Locate every Plasmodium parasite.
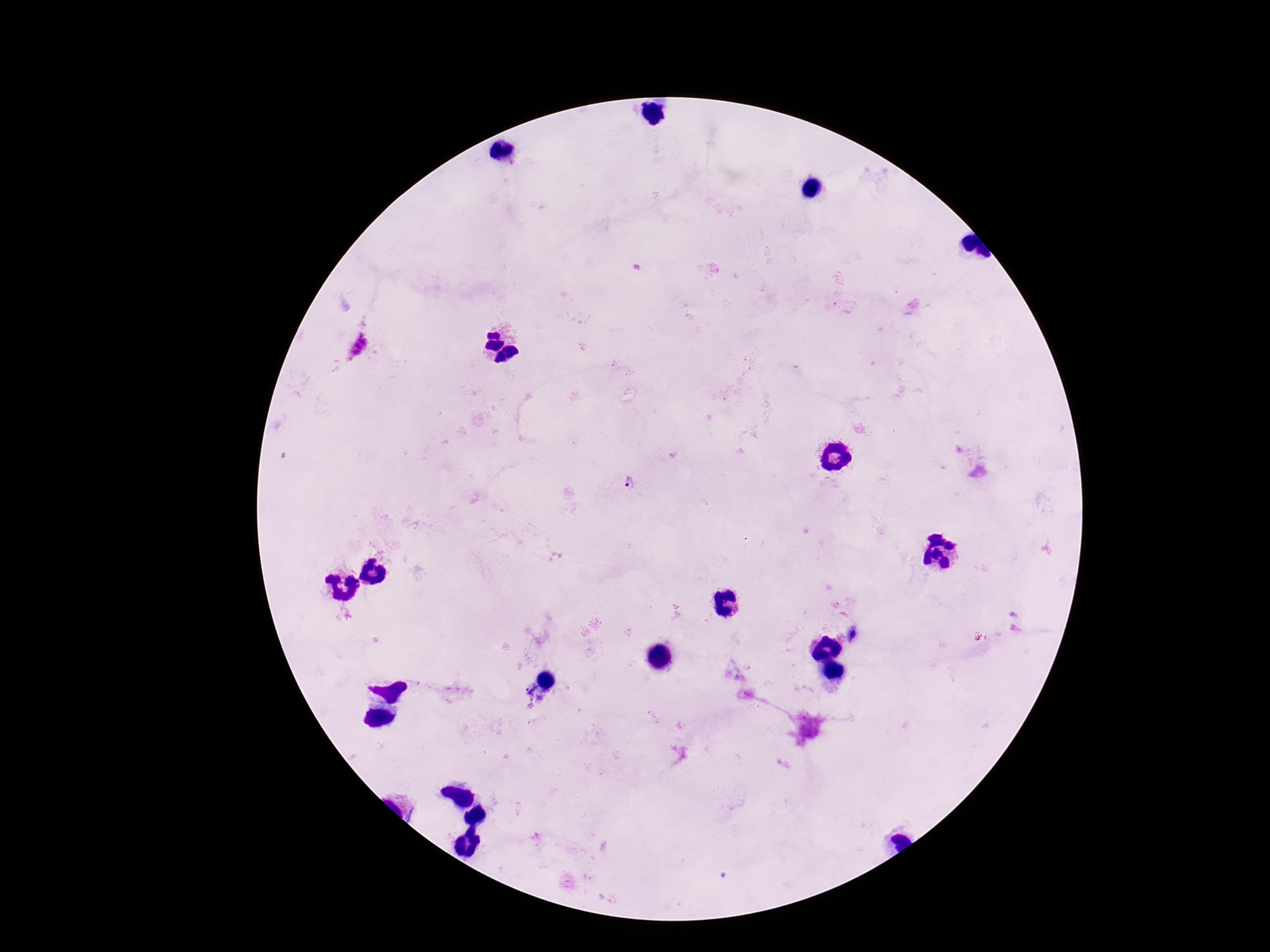
Approximate object centers, in pixels from the top-left corner.
Plasmodium parasites: (x=358, y=347), (x=630, y=484).

Single field of view. Photographed through the microscope eyepiece with a smartphone camera. Image is 1270×952 pixels. Giemsa stain. Thick blood film. 100x magnification. Patient malaria status: infected.